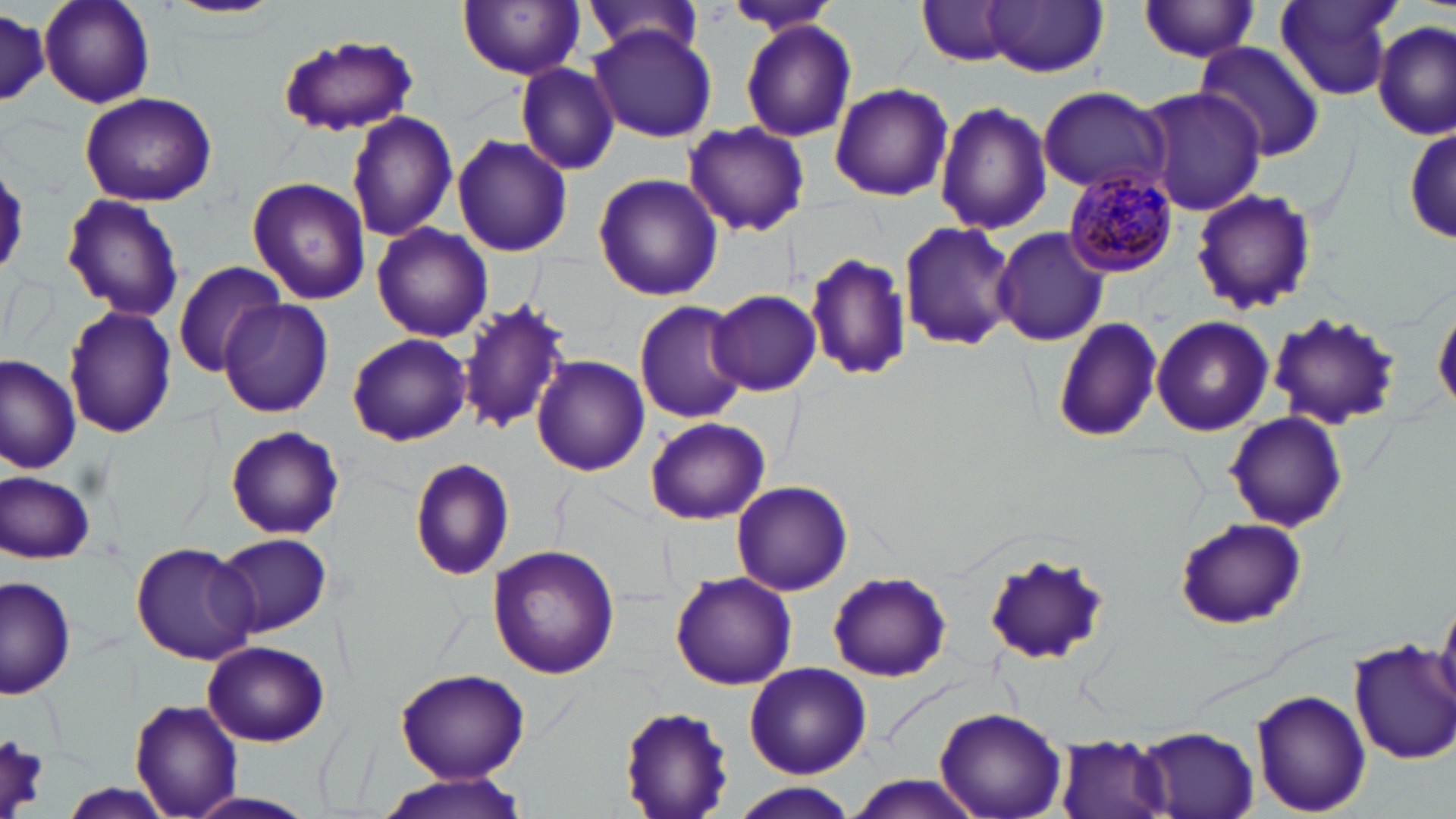
slide-level diagnosis = Plasmodium malariae
stain = May-Grünwald-Giemsa
uninfected red blood cell locations = approximate bounding boxes as [x1, y1, x2, y2] in pixels: [165, 0, 287, 22], [583, 0, 706, 62], [1272, 0, 1402, 103], [40, 1, 156, 109], [457, 1, 586, 79], [721, 1, 841, 38], [914, 1, 1022, 67], [984, 1, 1108, 77], [1136, 2, 1265, 63], [0, 10, 50, 112], [739, 21, 858, 141], [1373, 22, 1453, 139], [588, 24, 717, 142], [276, 34, 420, 139], [1195, 41, 1324, 159], [516, 63, 621, 175], [830, 83, 953, 201], [1036, 85, 1169, 196], [1137, 86, 1267, 213], [78, 90, 219, 207], [934, 101, 1052, 235], [346, 112, 459, 243], [685, 122, 810, 237], [1404, 124, 1455, 246], [450, 134, 575, 258], [593, 173, 724, 302], [247, 176, 371, 305], [1190, 188, 1318, 317], [59, 194, 186, 321], [896, 219, 1020, 353], [371, 223, 492, 343], [993, 226, 1108, 346], [806, 251, 912, 383], [173, 261, 285, 378], [708, 289, 821, 396], [458, 293, 572, 437], [217, 300, 334, 418], [1434, 301, 1456, 421], [634, 302, 750, 423], [64, 306, 179, 439], [1267, 312, 1404, 429], [1150, 315, 1274, 436], [1052, 318, 1162, 442], [347, 332, 472, 447], [1, 357, 81, 475], [533, 357, 649, 475], [1225, 411, 1349, 534], [645, 416, 768, 523], [225, 426, 345, 540], [411, 458, 516, 580], [2, 471, 96, 563], [731, 480, 854, 596], [1174, 516, 1306, 629], [214, 533, 333, 637], [129, 541, 259, 664], [487, 545, 620, 681], [982, 551, 1113, 669], [670, 571, 798, 690], [828, 572, 952, 683], [2, 575, 77, 701], [1436, 595, 1456, 707], [202, 640, 330, 747], [1350, 640, 1456, 763], [152, 659, 277, 780], [744, 662, 873, 779], [395, 667, 528, 782], [1251, 688, 1372, 816], [128, 699, 244, 819], [621, 703, 736, 817], [935, 706, 1065, 819], [1138, 727, 1258, 817], [1057, 733, 1176, 819], [0, 735, 49, 812], [373, 772, 533, 819], [843, 775, 986, 817], [55, 783, 180, 819], [733, 785, 856, 819], [182, 792, 319, 819]
preparation = thin blood film
field of view = one of a larger specimen
image size = 1456×819 pixels
modality = optical microscopy
Plasmodium malariae-infected red blood cell locations = approximate bounding boxes as [x1, y1, x2, y2] in pixels: [1064, 171, 1178, 276]
magnification = 1000x